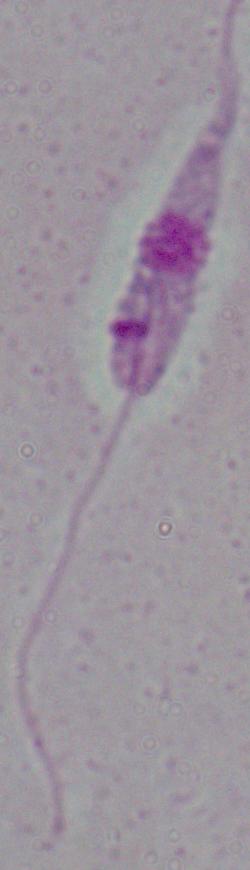
modality: micrograph
identification: Leishmania
magnification: 1000x